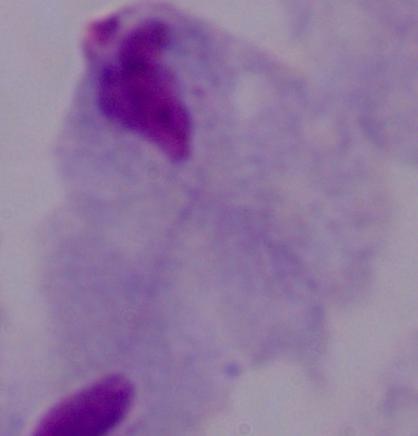

Summary:
  - Modality: micrograph
  - Identification: trichomonad
  - Magnification: 1000x